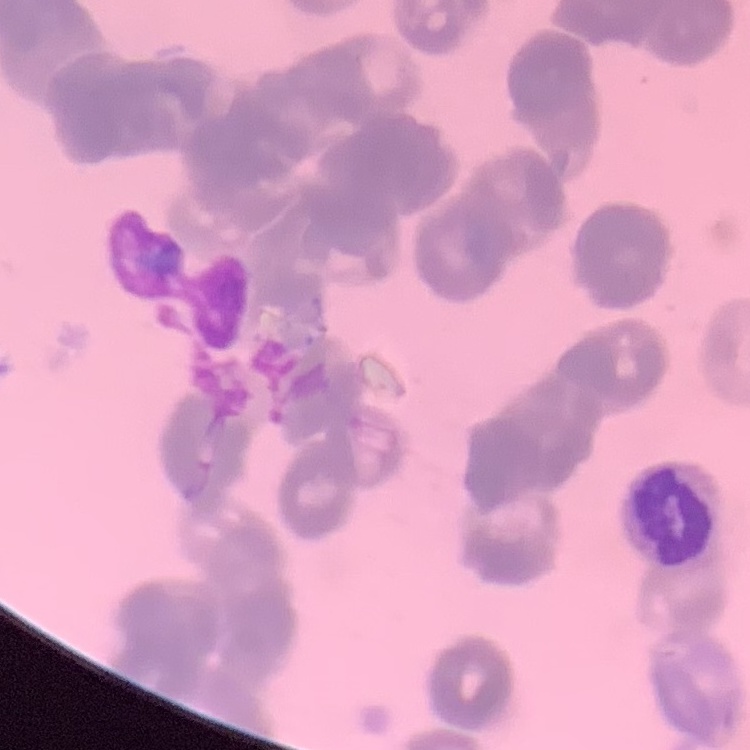

{
  "erythrocyte_morphology": "rouleaux formation",
  "stain": "Field's or Giemsa",
  "preparation": "thin blood film",
  "image_type": "one tile cut from a larger photomicrograph"
}